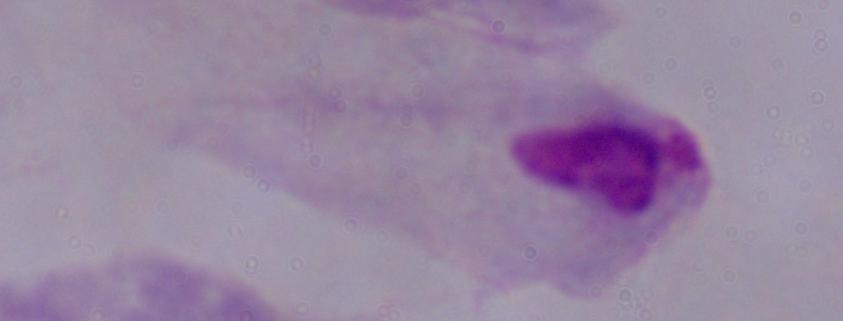
1000x magnification. A trichomonad is seen. Micrograph.